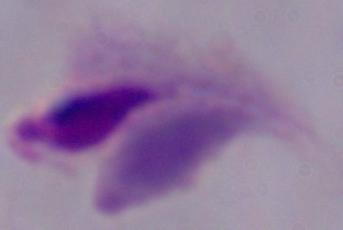
Summary:
  - Modality: photomicrograph
  - Magnification: 1000x
  - Identification: trichomonad